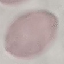

malaria_status: uninfected
image_type: cell patch, automatically extracted from a larger field of view and resized to 64 × 64 pixels
preparation: thin smear
capture: smartphone through the microscope eyepiece
stain: Giemsa